Locate every Plasmodium parasite.
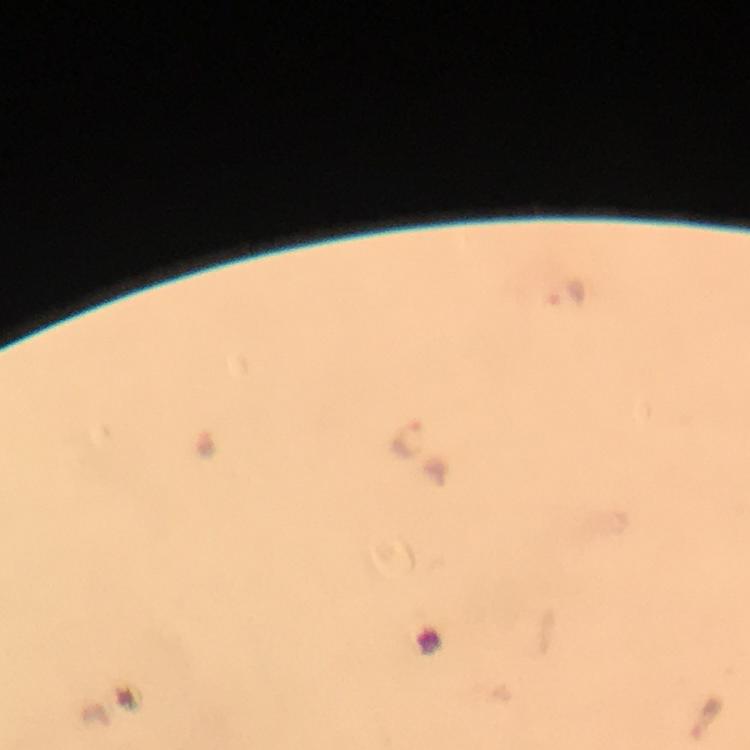

Approximate centers as [x, y] in pixels.
Plasmodium parasites: [567, 295], [408, 437].

Immersion oil applied. 100x magnification. Photographed with a smartphone mounted on the microscope. Image is 750×750 pixels. Giemsa-stained preparation. From a malaria diagnostic workup. Cropped region of a single field of view. Thick blood smear.